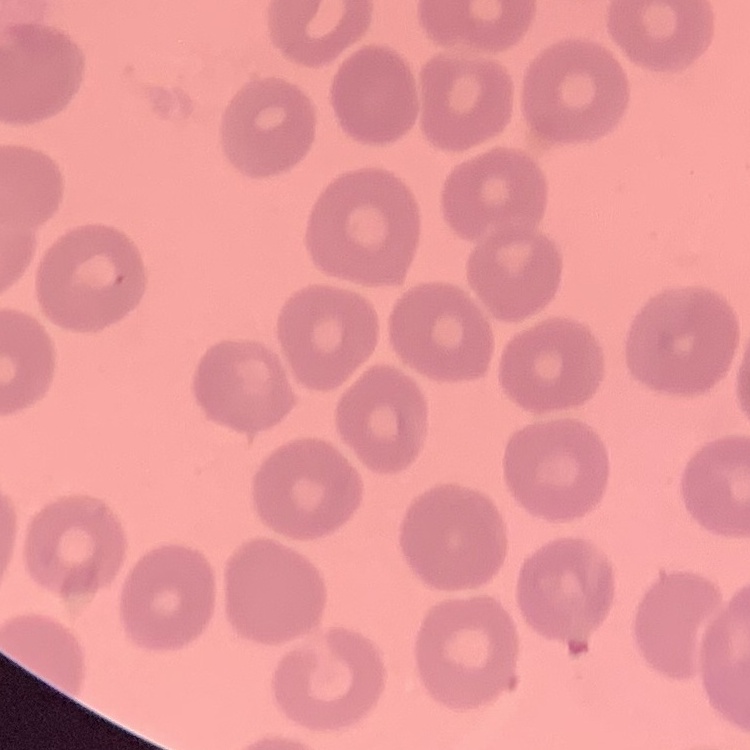

erythrocyte morphology = no rouleaux formation
preparation = thin peripheral smear
image type = square crop of a larger photomicrograph
stain = Field's or Giemsa